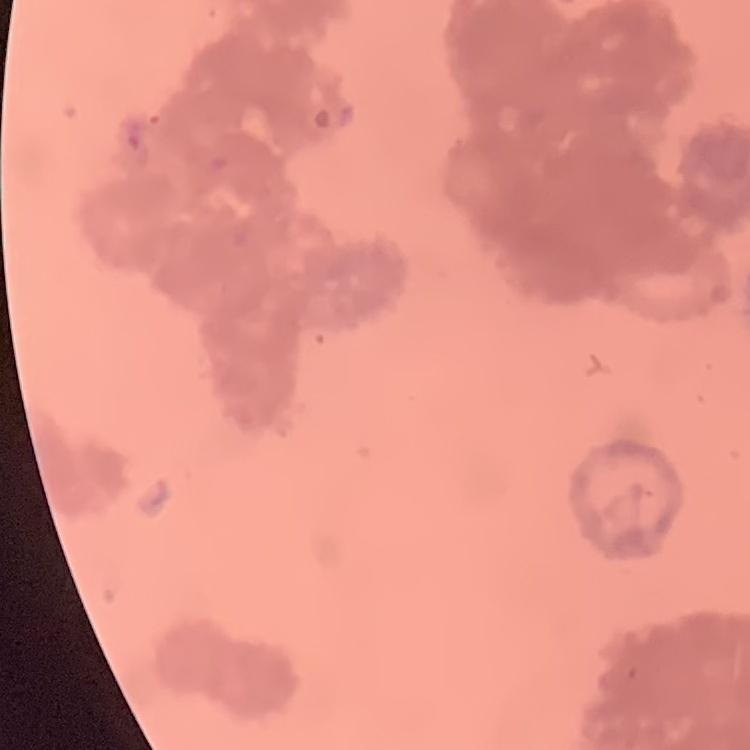

red_blood_cell_morphology: rouleaux formation
preparation: thin peripheral smear
image_type: square crop of a larger photomicrograph
stain: Field's or Giemsa